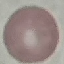 Result: negative for malaria parasites. Giemsa-stained preparation. Cell patch, automatically extracted from a larger field of view and resized to 64 × 64 pixels. Thin blood film. Photographed with a smartphone camera at the microscope eyepiece.